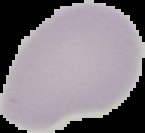

Malaria status: uninfected. Image is 145×133 pixels. Cell region segmented out of the field of view; the surrounding area is masked to black. From a thin blood film.